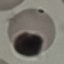

Malaria status: uninfected. Giemsa stain. Thin blood smear. Automatically extracted cell patch, resized to 64 × 64 pixels. Acquired by smartphone through the microscope eyepiece.